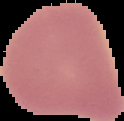
From a thin blood smear. Image is 124×121 pixels. Result: no Plasmodium parasites seen. Segmented cell region on a black background.